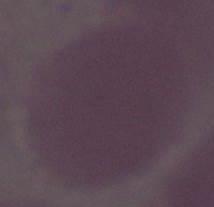

Summary:
  - Magnification: 1000x
  - Identification: erythrocyte
  - Modality: photomicrograph